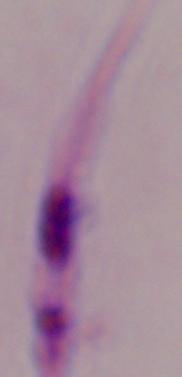
Summary:
  - Magnification: 1000x
  - Identification: Leishmania
  - Modality: micrograph